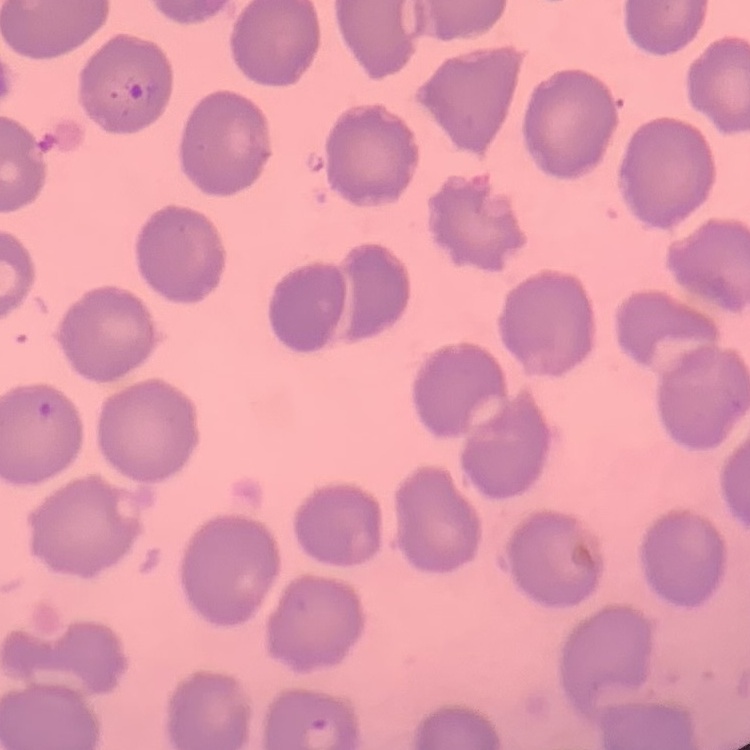

erythrocyte morphology = no rouleaux formation
image type = one tile cut from a larger photomicrograph
preparation = thin peripheral smear
stain = Field's or Giemsa